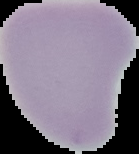

preparation: thin blood smear
image_type: segmented cell region on a black background
image_size: 139×154 pixels
malaria_status: uninfected